Assess this cell for malaria.
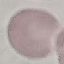

It is uninfected.

Acquired by smartphone through the microscope eyepiece. Giemsa-stained preparation. Cell patch, automatically extracted from a larger field of view and resized to 64 × 64 pixels. Thin blood smear.